Name the parasite shown.
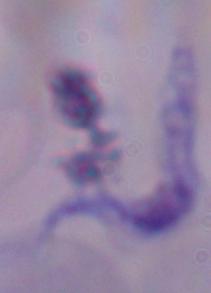

A trypanosome.

magnification = 1000x
modality = photomicrograph